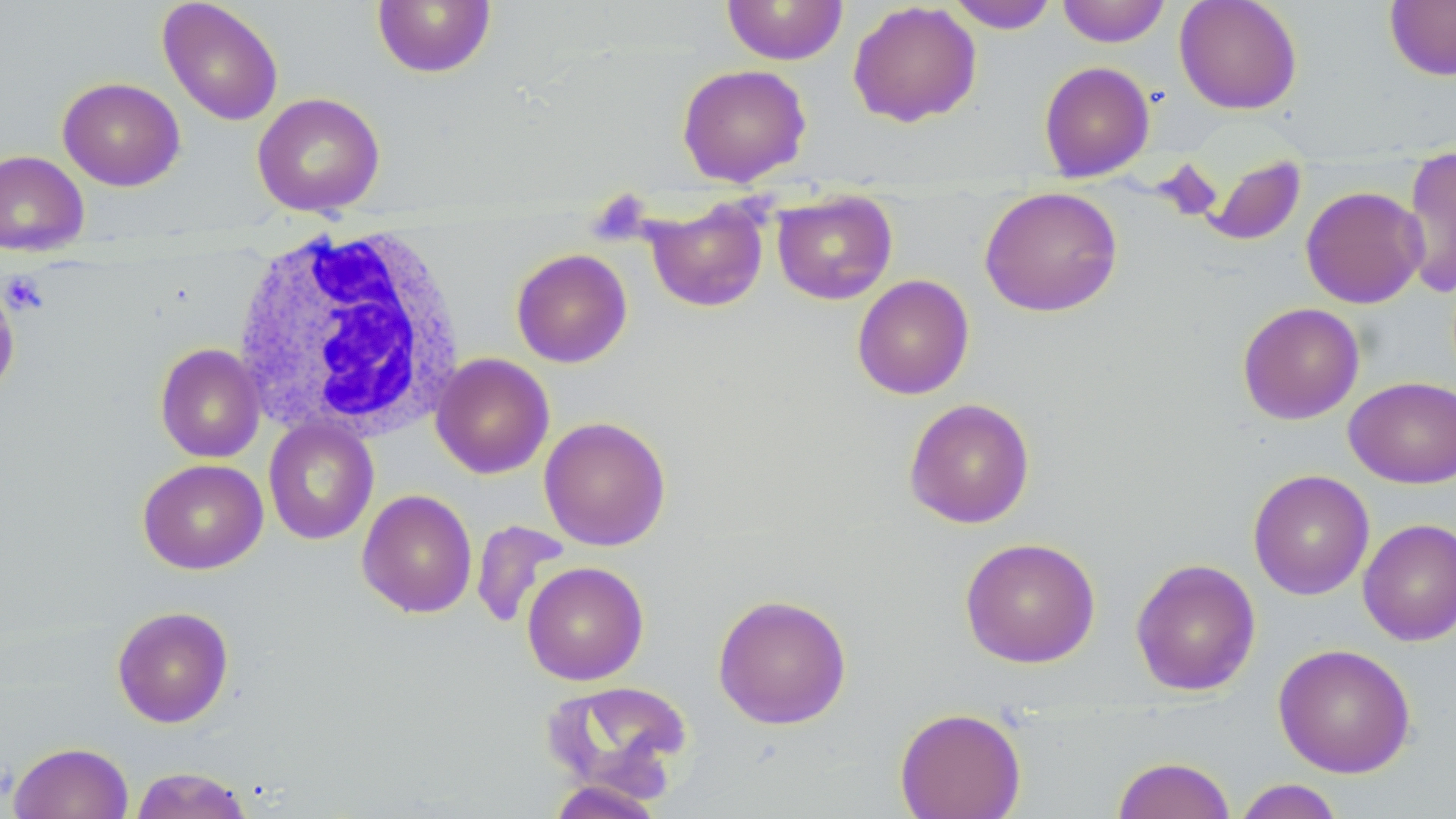

Summary:
  - Coordinate format: approximate bounding boxes as (x1, y1, x2, y2) in pixels
  - Uninfected red blood cell locations (subset): (722, 0, 848, 65), (1057, 0, 1170, 47), (1174, 0, 1302, 115), (1384, 0, 1456, 81), (158, 1, 284, 126), (372, 1, 497, 78), (945, 1, 1059, 34), (847, 2, 982, 127), (1039, 61, 1155, 182), (676, 63, 812, 187), (57, 77, 185, 191), (252, 92, 385, 216), (0, 149, 89, 256), (1400, 150, 1456, 300), (1203, 154, 1306, 246), (1300, 185, 1428, 309), (979, 186, 1123, 317), (771, 191, 898, 305), (644, 198, 770, 313), (511, 248, 633, 368), (852, 274, 974, 400), (0, 281, 20, 398), (1237, 302, 1364, 424), (155, 342, 265, 462), (430, 353, 554, 478), (1345, 377, 1456, 488), (903, 397, 1036, 528), (539, 416, 671, 551), (263, 418, 379, 545), (137, 458, 268, 575), (1248, 469, 1375, 600), (357, 488, 478, 618), (1358, 517, 1456, 647), (471, 520, 569, 630), (959, 537, 1101, 668), (1130, 558, 1261, 696), (522, 561, 649, 686), (712, 593, 852, 730), (112, 605, 234, 727), (1273, 643, 1417, 778), (543, 680, 694, 798), (894, 707, 1026, 819), (9, 742, 134, 819), (1112, 756, 1236, 819), (128, 766, 254, 819), (1233, 779, 1346, 819), (544, 780, 666, 819)
  - White blood cell locations: (229, 222, 468, 441)
  - Platelet locations (subset): (2, 271, 49, 315)
  - Slide-level diagnosis: no evidence of blood parasites
  - Modality: optical microscopy
  - Field of view: single
  - Image size: 1456×819 pixels
  - Stain: May-Grünwald-Giemsa
  - Magnification: 1000x
  - Preparation: thin blood film